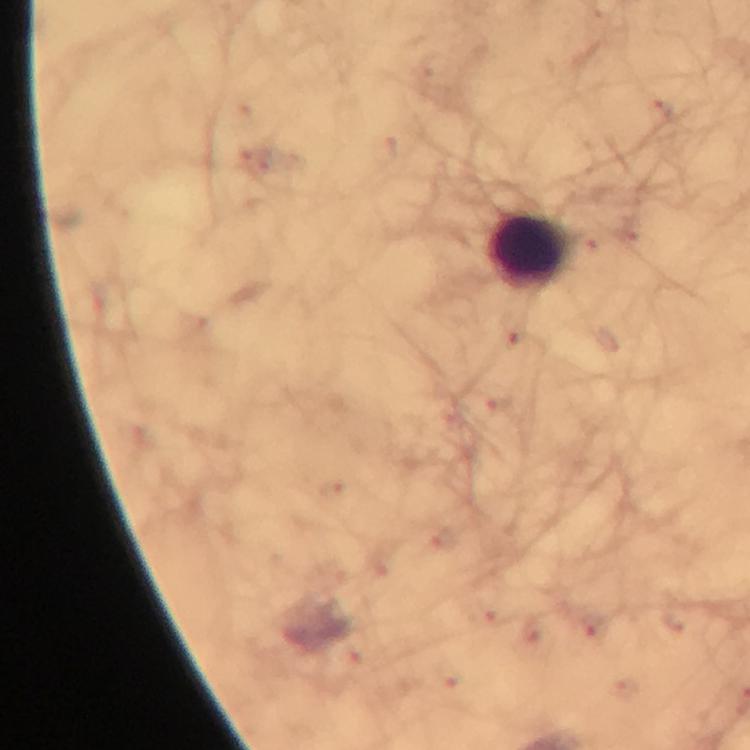

{
  "cropped_from": "one field of view",
  "context": "from a diagnostic examination for malaria",
  "preparation": "thick blood smear",
  "capture": "smartphone photograph through a microscope",
  "stain": "Giemsa",
  "malaria_parasites": "none detected",
  "leukocyte_locations": "approximate centers as [x, y] in pixels: [527, 250]",
  "magnification": "100x",
  "image_size": "750×750 pixels",
  "immersion_oil": "applied"
}